State which cell type is depicted.
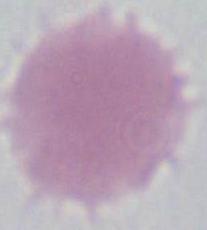
This is an erythrocyte.

1000x magnification. Micrograph.